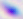
Summary:
  - Modality: micrograph
  - Magnification: 400x
  - Identification: Toxoplasma gondii